Assess this cell for malaria.
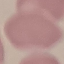

Uninfected.

Summary:
  - Capture: smartphone through the microscope eyepiece
  - Stain: Giemsa
  - Preparation: thin blood film
  - Image type: cell patch, automatically extracted from a larger field of view and resized to 64 × 64 pixels